Classify this cell by malaria status.
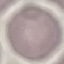

Uninfected.

image_type: cell patch, automatically extracted from a larger field of view and resized to 64 × 64 pixels
capture: smartphone through the microscope eyepiece
stain: Giemsa
preparation: thin blood smear